Report the malaria status of this cell.
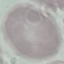

Uninfected.

Summary:
  - Preparation: thin smear
  - Capture: smartphone camera at the microscope eyepiece
  - Stain: Giemsa
  - Image type: automatically extracted cell patch, resized to 64 × 64 pixels